Outline each blood parasite and name the species.
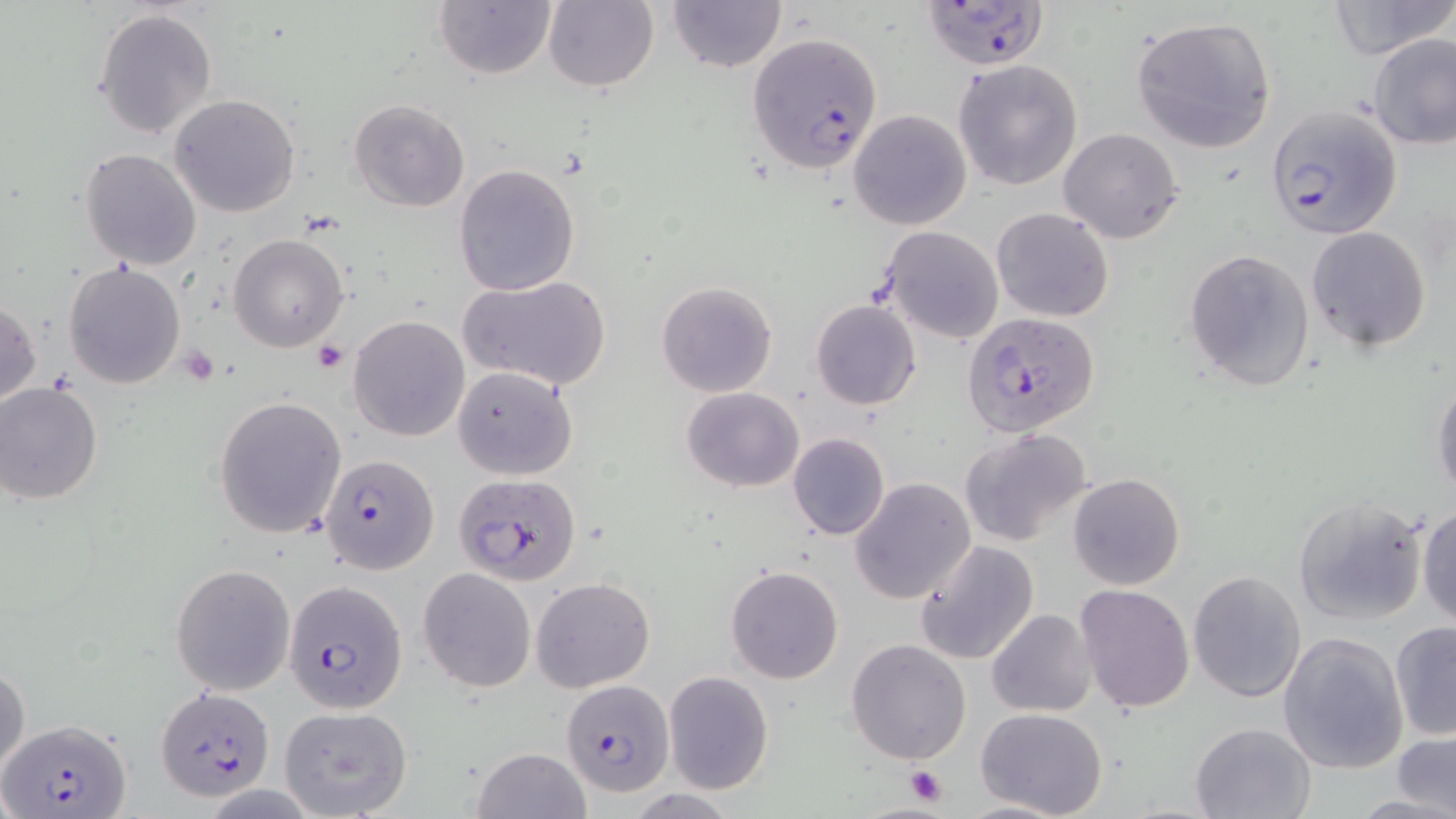
Approximate bounding boxes as named x1/y1/x2/y2 corners in pixels.
Plasmodium falciparum-infected red blood cells: (x1=921, y1=2, x2=1050, y2=70), (x1=746, y1=32, x2=884, y2=174), (x1=1266, y1=104, x2=1401, y2=242), (x1=963, y1=310, x2=1100, y2=438), (x1=320, y1=452, x2=439, y2=575), (x1=453, y1=472, x2=582, y2=584), (x1=285, y1=581, x2=407, y2=713), (x1=560, y1=680, x2=675, y2=799), (x1=157, y1=688, x2=275, y2=799), (x1=3, y1=721, x2=130, y2=816).
No Plasmodium ovale, Plasmodium malariae, Plasmodium vivax, Babesia divergens, or Trypanosoma brucei observed.

Summary:
  - Platelet locations: (x1=313, y1=342, x2=350, y2=373), (x1=178, y1=346, x2=218, y2=385), (x1=903, y1=765, x2=947, y2=807)
  - Uninfected red blood cell locations: (x1=665, y1=0, x2=786, y2=72), (x1=1328, y1=0, x2=1456, y2=61), (x1=434, y1=1, x2=557, y2=80), (x1=541, y1=1, x2=659, y2=91), (x1=93, y1=7, x2=217, y2=138), (x1=1131, y1=15, x2=1277, y2=153), (x1=1367, y1=33, x2=1456, y2=149), (x1=953, y1=59, x2=1083, y2=191), (x1=170, y1=94, x2=298, y2=217), (x1=349, y1=99, x2=472, y2=213), (x1=849, y1=109, x2=972, y2=230), (x1=1059, y1=128, x2=1184, y2=243), (x1=80, y1=147, x2=202, y2=269), (x1=453, y1=163, x2=581, y2=297), (x1=991, y1=207, x2=1114, y2=323), (x1=880, y1=226, x2=1005, y2=345), (x1=1306, y1=226, x2=1432, y2=350), (x1=228, y1=234, x2=347, y2=352), (x1=1184, y1=247, x2=1315, y2=392), (x1=63, y1=260, x2=185, y2=390), (x1=460, y1=275, x2=610, y2=390), (x1=656, y1=281, x2=779, y2=398), (x1=0, y1=296, x2=41, y2=411), (x1=811, y1=299, x2=921, y2=410), (x1=349, y1=315, x2=469, y2=441), (x1=452, y1=365, x2=578, y2=481), (x1=1431, y1=375, x2=1456, y2=499), (x1=0, y1=384, x2=103, y2=504), (x1=681, y1=386, x2=803, y2=492), (x1=213, y1=397, x2=349, y2=539), (x1=958, y1=427, x2=1092, y2=547), (x1=788, y1=432, x2=889, y2=541), (x1=1067, y1=473, x2=1185, y2=591), (x1=849, y1=478, x2=976, y2=604), (x1=1292, y1=494, x2=1428, y2=626), (x1=1416, y1=504, x2=1456, y2=629), (x1=914, y1=541, x2=1041, y2=665), (x1=171, y1=564, x2=295, y2=695), (x1=724, y1=565, x2=844, y2=685), (x1=418, y1=569, x2=536, y2=691), (x1=1188, y1=569, x2=1306, y2=702), (x1=530, y1=576, x2=655, y2=693), (x1=1075, y1=585, x2=1194, y2=714), (x1=986, y1=609, x2=1096, y2=717), (x1=1389, y1=621, x2=1455, y2=741), (x1=1277, y1=631, x2=1408, y2=774), (x1=846, y1=639, x2=972, y2=767), (x1=1, y1=661, x2=29, y2=778), (x1=663, y1=670, x2=774, y2=794), (x1=279, y1=707, x2=413, y2=819), (x1=974, y1=708, x2=1109, y2=819), (x1=1189, y1=721, x2=1316, y2=818), (x1=1394, y1=730, x2=1456, y2=817), (x1=472, y1=747, x2=591, y2=819)
  - Slide-level diagnosis: Plasmodium falciparum
  - Magnification: 1000x
  - Field of view: single
  - Modality: light microscopy
  - Image size: 1456×819 pixels
  - Stain: May-Grünwald-Giemsa
  - Preparation: thin blood smear